Classify this cell by malaria status.
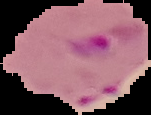
It is parasitized.

{
  "image_size": "151×115 pixels",
  "preparation": "thin blood smear",
  "image_type": "segmented cell region with the area outside set to black"
}